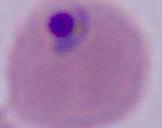
Captured at either 400x or 1000x magnification. A Plasmodium parasite is seen. Photomicrograph.